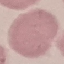
result = negative for malaria parasites
preparation = thin blood film
stain = Giemsa
image type = cell patch, automatically extracted from a larger field of view and resized to 64 × 64 pixels
capture = smartphone camera at the microscope eyepiece